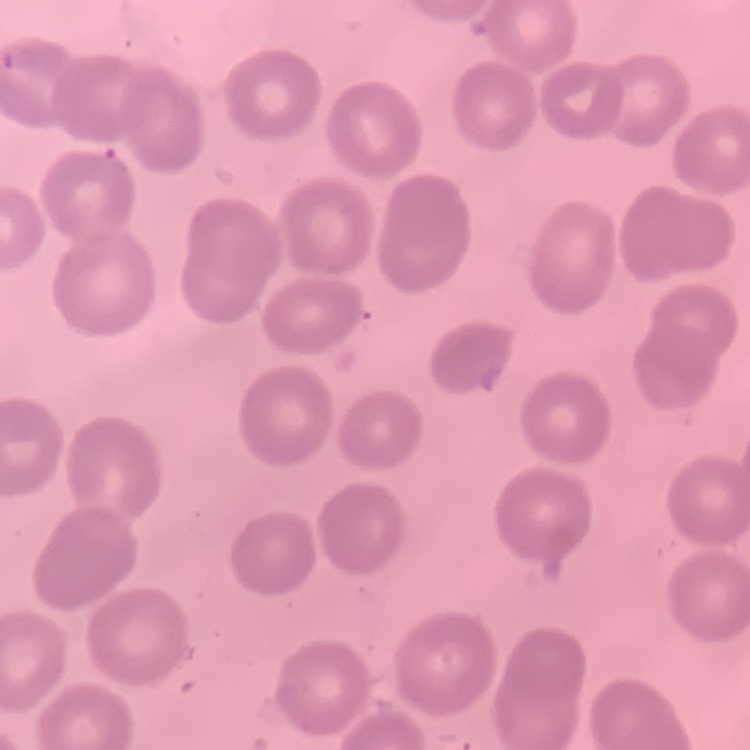
The red blood cells exhibit no rouleaux formation. Square crop of a larger photomicrograph. Stained with either Field's or Giemsa. Thin blood film.